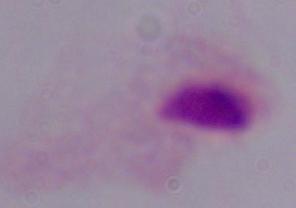
modality: photomicrograph
magnification: 1000x
identification: trichomonad